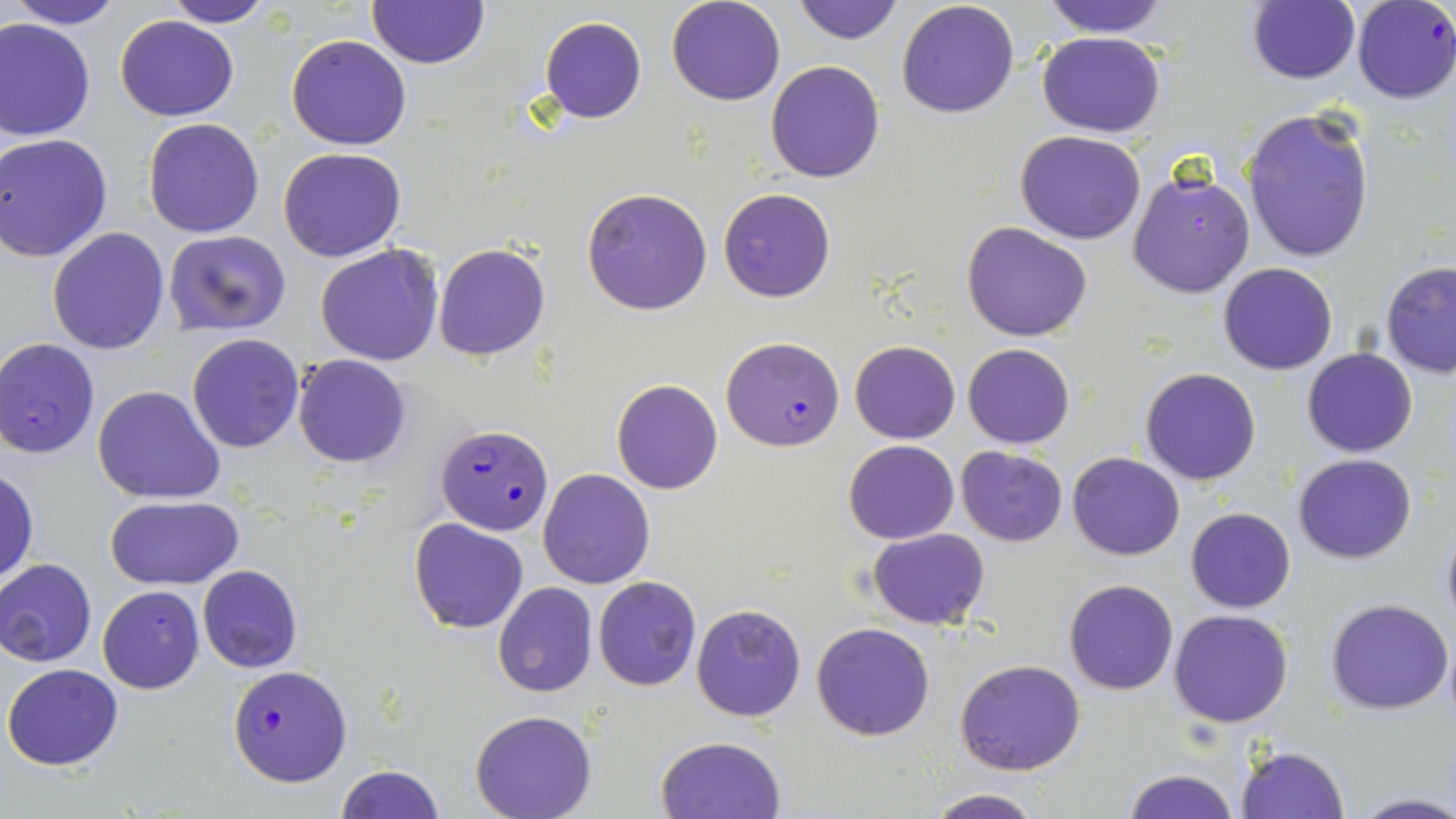
Summary:
  - Coordinate format: approximate bounding boxes as [x1, y1, x2, y2] in pixels
  - Uninfected red blood cell locations: [5, 0, 128, 29], [162, 0, 279, 26], [666, 0, 786, 106], [790, 0, 906, 46], [1039, 0, 1171, 39], [1247, 0, 1361, 85], [368, 1, 489, 69], [896, 1, 1020, 119], [539, 15, 648, 124], [116, 16, 240, 122], [0, 18, 96, 141], [1037, 31, 1166, 138], [287, 34, 413, 150], [766, 60, 885, 184], [1241, 105, 1374, 265], [143, 117, 266, 238], [1015, 130, 1145, 244], [2, 133, 115, 263], [278, 147, 405, 262], [1128, 169, 1255, 299], [582, 188, 713, 314], [717, 188, 836, 303], [962, 222, 1092, 341], [47, 226, 171, 355], [164, 230, 291, 336], [315, 242, 445, 366], [433, 243, 549, 360], [1380, 261, 1456, 378], [1218, 262, 1338, 376], [187, 333, 305, 453], [849, 340, 960, 443], [963, 343, 1075, 448], [1302, 347, 1418, 458], [292, 354, 412, 468], [1139, 367, 1262, 486], [612, 379, 723, 495], [92, 384, 224, 503], [844, 439, 959, 544], [956, 447, 1069, 546], [1067, 451, 1184, 560], [1293, 453, 1418, 564], [1, 468, 38, 583], [538, 468, 655, 589], [104, 495, 245, 591], [1186, 507, 1295, 613], [1439, 518, 1456, 632], [408, 519, 530, 635], [867, 528, 991, 630], [0, 559, 97, 667], [197, 565, 304, 674], [593, 576, 701, 691], [1063, 579, 1178, 695], [492, 583, 598, 698], [97, 585, 204, 694], [1327, 598, 1452, 715], [690, 604, 807, 722], [1170, 609, 1293, 728], [811, 622, 936, 741], [1442, 630, 1455, 728], [955, 658, 1085, 776], [3, 663, 124, 769], [469, 711, 597, 819], [655, 736, 787, 819], [1234, 745, 1350, 819], [334, 764, 446, 819], [1122, 769, 1240, 819], [923, 790, 1046, 819], [1351, 794, 1456, 819]
  - Plasmodium falciparum-infected red blood cell locations: [1351, 0, 1456, 104], [721, 336, 845, 451], [1, 338, 101, 459], [437, 423, 554, 535], [227, 663, 350, 787]
  - Slide-level diagnosis: Plasmodium falciparum
  - Preparation: thin blood film
  - Stain: May-Grünwald-Giemsa
  - Image size: 1456×819 pixels
  - Field of view: single
  - Modality: light microscopy
  - Magnification: 1000x